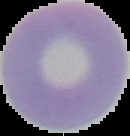 Segmented cell region on a black background. Image is 130×136 pixels. From a thin blood smear. Result: no Plasmodium parasites seen.